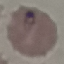

Summary:
  - Malaria status: parasitized
  - Stain: Giemsa
  - Capture: smartphone camera at the microscope eyepiece
  - Preparation: thin smear
  - Image type: automatically extracted cell patch, resized to 64 × 64 pixels